State the blood parasite species.
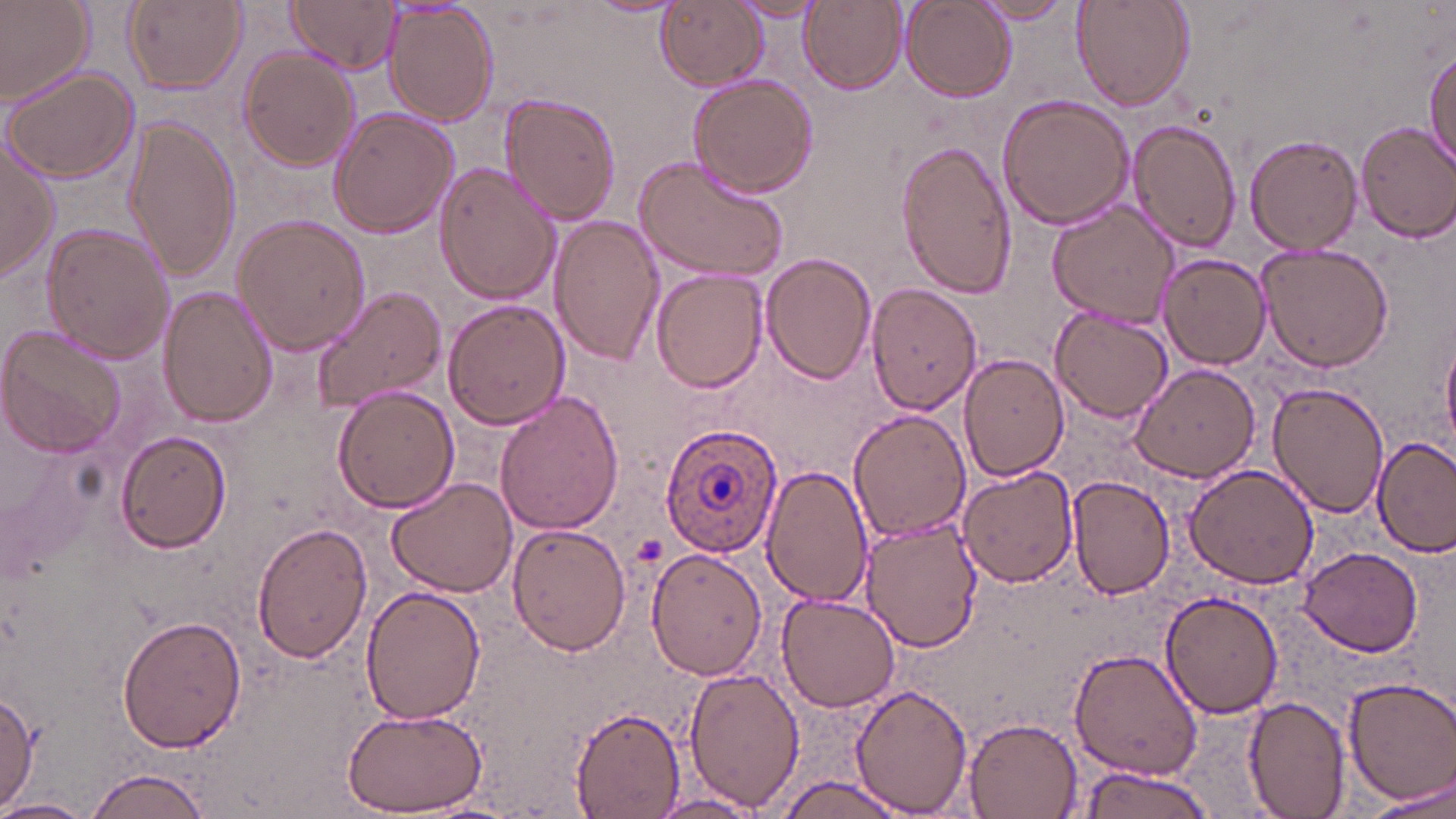
Plasmodium ovale.

Summary:
  - Coordinate format: approximate bounding boxes as (x1, y1, x2, y2) in pixels
  - Plasmodium ovale-infected red blood cell locations: (659, 423, 782, 557)
  - Uninfected red blood cell locations: (0, 0, 95, 108), (124, 0, 246, 95), (286, 0, 402, 73), (800, 0, 906, 95), (972, 0, 1078, 24), (1071, 0, 1195, 113), (655, 1, 767, 91), (732, 1, 827, 22), (901, 1, 1013, 102), (383, 3, 499, 126), (238, 48, 362, 170), (1424, 51, 1456, 169), (3, 65, 140, 185), (688, 71, 821, 198), (500, 93, 621, 226), (997, 93, 1136, 230), (328, 108, 459, 239), (124, 116, 242, 282), (1129, 119, 1241, 251), (1355, 121, 1456, 241), (1245, 133, 1363, 255), (893, 135, 1017, 299), (0, 137, 59, 284), (633, 153, 792, 282), (432, 163, 561, 306), (1048, 200, 1179, 328), (549, 213, 666, 367), (232, 214, 371, 356), (41, 223, 176, 365), (1257, 241, 1395, 373), (761, 253, 877, 384), (1158, 253, 1271, 369), (652, 269, 768, 392), (866, 283, 982, 415), (311, 284, 447, 415), (159, 286, 279, 427), (441, 300, 569, 429), (1051, 307, 1174, 422), (1, 324, 128, 458), (1441, 333, 1456, 457), (958, 354, 1068, 482), (1129, 361, 1261, 483), (1268, 380, 1391, 519), (332, 385, 460, 515), (494, 391, 624, 536), (848, 409, 970, 542), (116, 429, 233, 553), (1373, 436, 1456, 553), (1183, 462, 1320, 589), (760, 464, 874, 608), (956, 466, 1078, 589), (1067, 474, 1178, 599), (388, 478, 517, 597), (860, 518, 983, 652), (252, 522, 373, 665), (506, 524, 631, 657), (1297, 543, 1423, 658), (645, 547, 766, 681), (362, 584, 487, 727), (776, 591, 901, 714), (1161, 591, 1285, 720), (119, 611, 247, 755), (1068, 647, 1204, 780), (683, 667, 804, 811), (1340, 676, 1456, 806), (849, 683, 975, 814), (0, 692, 41, 813), (1242, 695, 1352, 818), (338, 703, 486, 817), (569, 705, 685, 817), (962, 718, 1082, 817), (1073, 764, 1216, 819), (84, 766, 217, 819), (775, 774, 910, 818), (1364, 779, 1456, 816), (649, 792, 762, 817), (0, 796, 96, 819)
  - Preparation: thin blood film
  - Magnification: 1000x
  - Stain: May-Grünwald-Giemsa
  - Modality: optical microscopy
  - Field of view: single
  - Image size: 1456×819 pixels